Outline each Trypanosoma brucei.
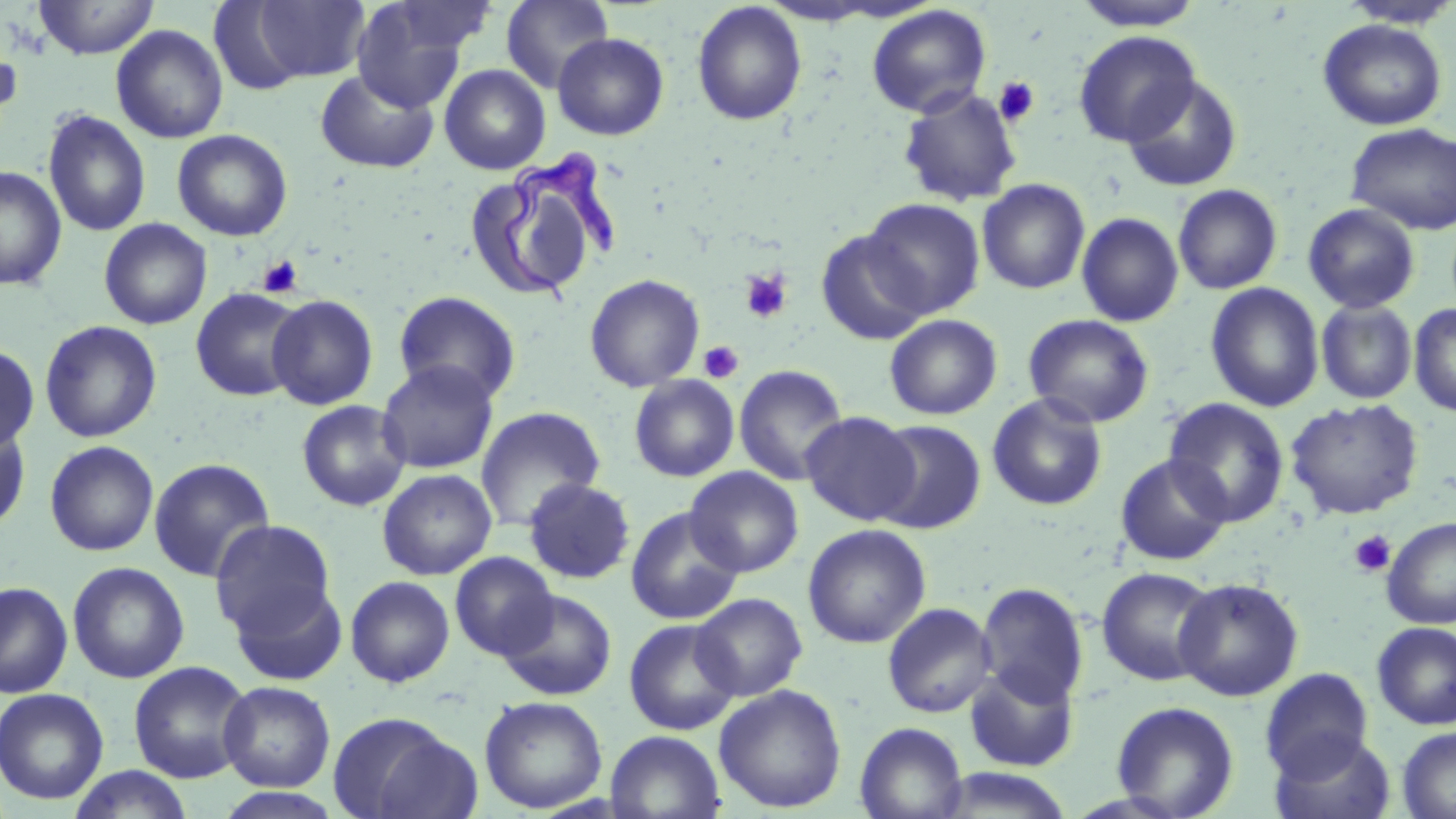

Approximate bounding boxes as [x1, y1, x2, y2] in pixels.
Trypanosoma brucei: [500, 144, 615, 305].

Platelet locations: [993, 76, 1040, 127], [258, 255, 304, 297], [739, 269, 793, 323], [698, 340, 744, 384], [1349, 530, 1396, 578]. Uninfected red blood cell locations: [33, 0, 159, 59], [382, 0, 497, 56], [501, 0, 614, 93], [1074, 0, 1204, 31], [245, 1, 371, 84], [350, 2, 471, 112], [692, 2, 807, 126], [1338, 3, 1454, 30], [866, 4, 991, 119], [1317, 19, 1447, 131], [111, 25, 228, 144], [1073, 30, 1201, 148], [0, 33, 22, 137], [552, 33, 669, 140], [439, 64, 550, 174], [314, 69, 439, 173], [1120, 74, 1243, 192], [897, 87, 1023, 208], [42, 109, 150, 237], [1346, 123, 1456, 234], [172, 129, 293, 241], [0, 166, 66, 291], [976, 178, 1090, 294], [467, 180, 583, 292], [1172, 183, 1283, 295], [862, 198, 985, 318], [1302, 203, 1421, 314], [1076, 212, 1184, 327], [98, 218, 212, 330], [816, 230, 931, 345], [584, 273, 705, 392], [1205, 283, 1324, 412], [190, 287, 307, 402], [393, 291, 521, 405], [267, 294, 379, 410], [1315, 300, 1417, 405], [1409, 302, 1456, 417], [1023, 313, 1155, 428], [884, 314, 1002, 420], [39, 320, 162, 443], [0, 342, 40, 454], [376, 360, 499, 474], [733, 364, 848, 485], [629, 375, 740, 482], [987, 392, 1108, 511], [1163, 398, 1289, 527], [1286, 398, 1423, 520], [296, 399, 411, 511], [475, 406, 606, 531], [801, 411, 921, 526], [0, 417, 32, 535], [871, 420, 987, 534], [44, 440, 159, 557], [1114, 453, 1232, 565], [148, 458, 275, 583], [685, 466, 804, 578], [377, 469, 497, 580], [523, 478, 636, 585], [625, 506, 743, 625], [1382, 517, 1456, 629], [209, 520, 337, 641], [802, 524, 931, 648], [450, 552, 559, 660], [67, 561, 190, 684], [1096, 566, 1219, 687], [345, 576, 455, 688], [1173, 577, 1304, 701], [228, 578, 349, 686], [0, 581, 73, 698], [977, 582, 1088, 707], [498, 589, 617, 701], [691, 592, 807, 701], [881, 602, 997, 718], [624, 618, 741, 735], [1371, 621, 1456, 730], [128, 661, 254, 783], [964, 664, 1081, 772], [1259, 667, 1374, 781], [219, 681, 335, 792], [714, 684, 847, 813], [0, 687, 109, 805], [479, 695, 608, 813], [1111, 700, 1239, 818], [328, 712, 476, 819], [854, 722, 968, 819], [1397, 726, 1456, 818], [605, 730, 725, 818], [1270, 731, 1396, 819], [67, 766, 195, 819], [932, 768, 1077, 819], [214, 787, 346, 818]. Slide-level diagnosis: Trypanosoma brucei. Light microscopy. Thin blood film. 1000x magnification. May-Grünwald-Giemsa-stained preparation. Image is 1456×819 pixels. One field of a larger specimen.